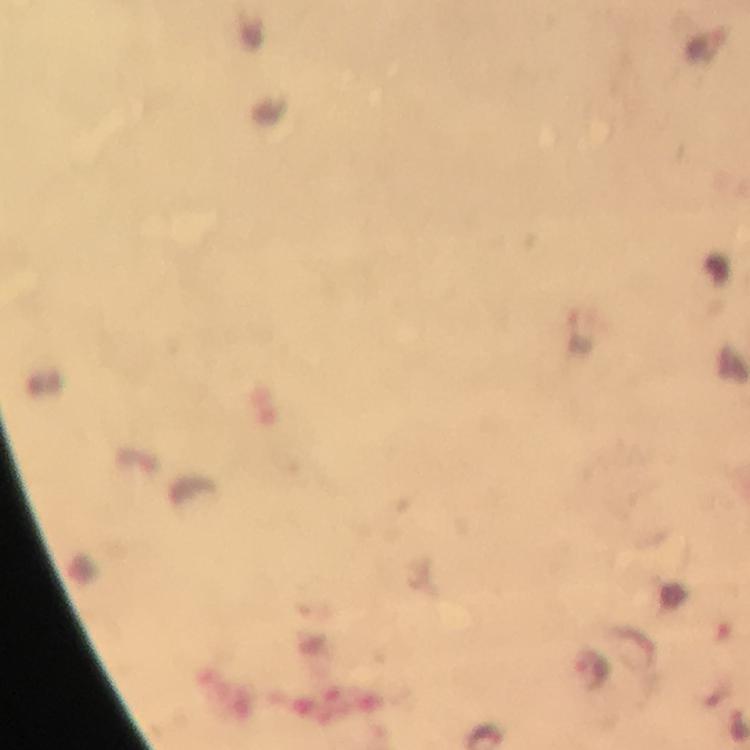 Approximate centers as {x, y} in pixels. Plasmodium parasite locations: {594, 671}. Giemsa stain. At 100x magnification. Thick smear. From a malaria diagnostic workup. Photographed through the microscope with a smartphone camera. Cropped region of a single field of view. Image is 750×750 pixels. Immersion oil applied.